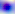
Toxoplasma gondii is seen. 400x magnification. Photomicrograph.